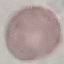

Result: no malaria parasites detected. Acquired by smartphone through the microscope eyepiece. Automatically extracted cell patch, resized to 64 × 64 pixels. Thin smear of blood. Giemsa-stained preparation.